Locate every Plasmodium falciparum-infected red blood cell.
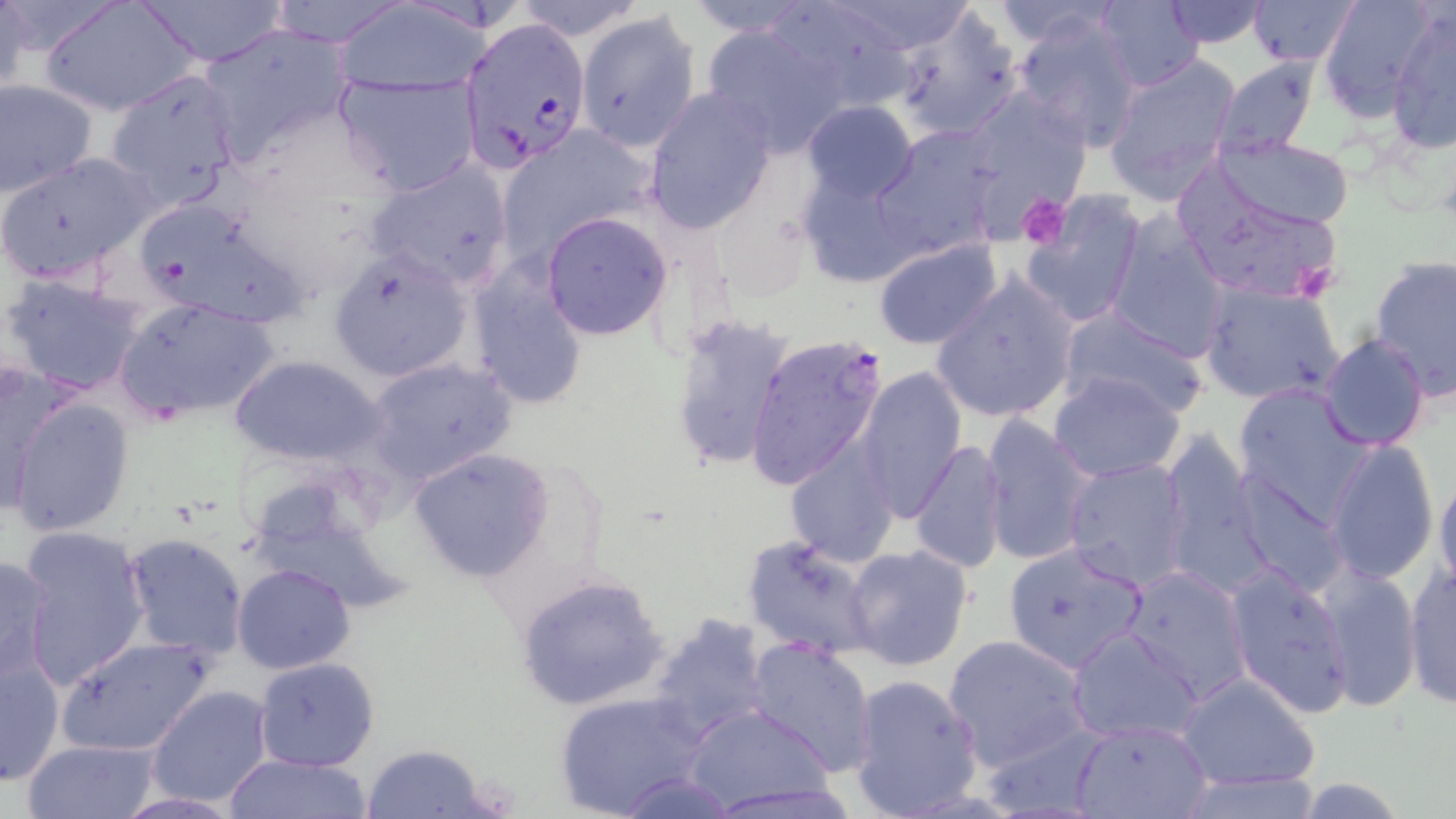
Approximate bounding boxes as (x1,y1)-(x2,y2) corner pairs in pixels.
Plasmodium falciparum-infected red blood cells: (464,19)-(595,174), (745,333)-(889,492).

slide-level diagnosis = Plasmodium falciparum
magnification = 1000x
uninfected red blood cell locations = approximate bounding boxes as (x1,y1)-(x2,y2) corner pairs in pixels: (40,0)-(199,115), (132,0)-(288,67), (263,0)-(410,48), (763,0)-(921,113), (1090,0)-(1205,91), (1159,0)-(1269,47), (1246,0)-(1359,67), (1316,0)-(1442,121), (333,1)-(491,97), (0,2)-(35,95), (888,4)-(1026,143), (1387,7)-(1456,153), (577,10)-(700,153), (1014,10)-(1142,151), (697,18)-(847,155), (199,21)-(354,161), (1102,52)-(1243,202), (1212,57)-(1321,159), (103,67)-(243,203), (333,72)-(481,197), (0,78)-(97,198), (644,87)-(777,233), (959,87)-(1089,218), (801,101)-(919,205), (870,126)-(1001,261), (498,131)-(647,265), (1212,135)-(1357,230), (0,150)-(154,285), (362,160)-(516,292), (795,163)-(922,292), (1179,179)-(1348,304), (1020,194)-(1146,327), (129,196)-(307,331), (541,211)-(674,341), (1105,216)-(1229,360), (872,237)-(1003,351), (328,249)-(474,384), (1368,256)-(1456,399), (467,259)-(590,411), (2,271)-(149,397), (929,271)-(1080,424), (1199,279)-(1346,408), (114,299)-(281,423), (1058,306)-(1210,418), (672,315)-(796,476), (1319,333)-(1431,452), (229,353)-(387,468), (365,357)-(517,485), (0,359)-(74,515), (855,365)-(967,518), (1048,372)-(1187,481), (1232,382)-(1373,522), (5,396)-(135,538), (980,414)-(1096,567), (1159,429)-(1266,594), (910,438)-(1008,576), (1323,439)-(1438,583), (784,442)-(899,565), (408,447)-(555,582), (1062,458)-(1190,592), (1434,468)-(1456,598), (1233,473)-(1346,596), (16,527)-(151,687), (121,532)-(250,661), (740,533)-(881,661), (1002,542)-(1150,675), (842,544)-(975,672), (0,554)-(57,686), (1224,563)-(1356,717), (232,564)-(356,676), (1402,564)-(1456,710), (1121,565)-(1251,701), (1316,565)-(1422,711), (515,571)-(670,713), (646,612)-(775,746), (1067,625)-(1205,744), (944,633)-(1093,773), (58,636)-(214,757), (745,637)-(877,774), (1,649)-(65,787), (254,657)-(380,771), (1174,671)-(1322,791), (848,672)-(985,819), (147,685)-(273,805), (554,691)-(711,817), (681,703)-(839,812), (1074,719)-(1211,818), (20,739)-(161,819), (358,744)-(494,818), (224,753)-(377,818), (616,772)-(740,818), (1178,772)-(1329,818), (1289,777)-(1411,818)
platelet locations = approximate bounding boxes as (x1,y1)-(x2,y2) corner pairs in pixels: (1017,194)-(1072,251)
field of view = one of a larger specimen
preparation = thin blood smear
image size = 1456×819 pixels
stain = May-Grünwald-Giemsa
modality = light microscopy